Outline each Plasmodium ovale-infected red blood cell.
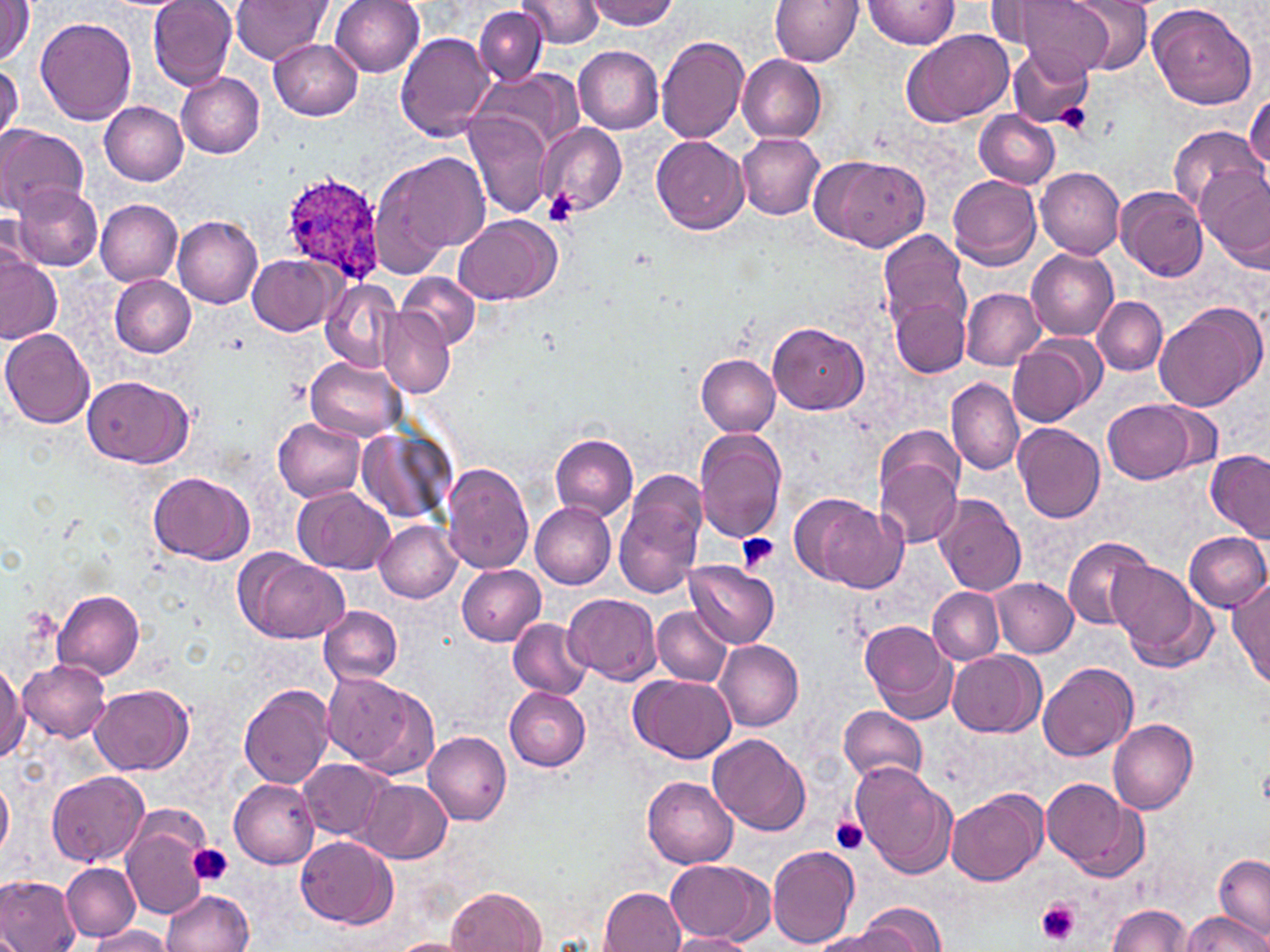

Approximate bounding boxes as (x1, y1, x2, y2) in pixels.
Plasmodium ovale-infected red blood cells: (279, 173, 389, 288).

{
  "slide_level_diagnosis": "Plasmodium ovale",
  "image_size": "1270×952 pixels",
  "platelet_locations": "approximate bounding boxes as (x1, y1, x2, y2) in pixels: (1058, 103, 1092, 134), (542, 188, 580, 226), (736, 534, 779, 570), (830, 818, 869, 854), (189, 844, 232, 886), (1035, 899, 1081, 945)",
  "field_of_view": "single",
  "magnification": "1000x",
  "preparation": "thin blood film",
  "stain": "May-Grünwald-Giemsa",
  "uninfected_red_blood_cell_locations": "approximate bounding boxes as (x1, y1, x2, y2) in pixels: (0, 0, 34, 66), (149, 0, 237, 90), (231, 0, 331, 64), (330, 0, 425, 76), (519, 0, 607, 48), (584, 0, 679, 30), (770, 0, 862, 65), (861, 0, 961, 48), (1007, 0, 1115, 79), (1061, 0, 1155, 75), (1147, 2, 1260, 108), (474, 5, 546, 85), (36, 17, 136, 125), (901, 28, 1014, 126), (396, 32, 496, 140), (655, 35, 750, 143), (270, 39, 363, 120), (573, 45, 663, 134), (1006, 45, 1096, 129), (738, 55, 827, 142), (0, 63, 23, 145), (469, 66, 580, 159), (177, 72, 264, 159), (1246, 92, 1269, 182), (99, 102, 188, 185), (975, 110, 1060, 189), (465, 113, 553, 217), (536, 122, 627, 216), (0, 124, 88, 217), (1169, 125, 1262, 214), (736, 134, 825, 219), (652, 135, 748, 234), (374, 149, 489, 268), (812, 154, 926, 250), (1195, 166, 1269, 264), (1036, 167, 1124, 260), (947, 176, 1041, 270), (11, 182, 104, 271), (1115, 186, 1209, 281), (96, 199, 182, 285), (1, 213, 40, 280), (455, 214, 560, 304), (174, 215, 263, 307), (878, 229, 971, 333), (1027, 249, 1118, 340), (0, 253, 62, 345), (249, 255, 339, 335), (109, 273, 197, 356), (397, 273, 480, 350), (321, 278, 403, 372), (962, 289, 1045, 369), (891, 295, 971, 376), (1094, 298, 1167, 375), (1153, 301, 1267, 411), (377, 309, 455, 398), (768, 321, 869, 415), (0, 328, 94, 429), (1009, 335, 1102, 428), (697, 353, 781, 435), (307, 356, 406, 441), (82, 374, 193, 469), (947, 377, 1023, 476), (1103, 397, 1197, 483), (274, 416, 365, 503), (358, 423, 455, 523), (1012, 423, 1104, 522), (694, 428, 787, 545), (550, 434, 638, 521), (1206, 450, 1270, 542), (873, 452, 964, 550), (441, 463, 533, 573), (613, 470, 709, 600), (148, 472, 253, 563), (293, 487, 393, 574), (935, 493, 1027, 596), (801, 495, 904, 592), (530, 504, 616, 588), (374, 520, 462, 603), (1184, 531, 1270, 612), (1062, 535, 1156, 630), (239, 553, 349, 643), (685, 561, 780, 647), (1110, 562, 1214, 672), (456, 565, 546, 645), (1228, 575, 1270, 690), (992, 578, 1078, 657), (928, 588, 1002, 663), (53, 590, 146, 680), (564, 593, 662, 685), (319, 606, 403, 685), (653, 606, 732, 686), (507, 619, 592, 698), (861, 620, 957, 722), (714, 640, 804, 732), (947, 651, 1042, 736), (19, 659, 112, 741), (1038, 659, 1136, 760), (0, 661, 27, 761), (323, 674, 420, 769), (631, 675, 735, 764), (240, 684, 338, 788), (91, 685, 193, 775), (503, 686, 591, 770), (839, 705, 927, 783), (1108, 718, 1198, 815), (424, 732, 512, 825), (708, 732, 811, 836), (300, 757, 394, 841), (851, 762, 957, 880), (46, 771, 150, 868), (0, 775, 14, 859), (642, 776, 739, 867), (229, 778, 321, 867), (1042, 778, 1145, 880), (361, 779, 452, 863), (945, 789, 1045, 885), (122, 815, 210, 920), (296, 835, 397, 929), (767, 845, 861, 948), (1215, 853, 1269, 940), (663, 858, 773, 944), (60, 862, 140, 941), (1, 876, 82, 952), (448, 886, 546, 952), (600, 887, 686, 951), (162, 888, 254, 952), (852, 902, 947, 952), (1106, 905, 1194, 951), (1182, 913, 1267, 952), (89, 926, 172, 951), (814, 928, 915, 952), (669, 932, 754, 952), (385, 937, 473, 952)",
  "modality": "optical microscopy"
}